Give the preparation type.
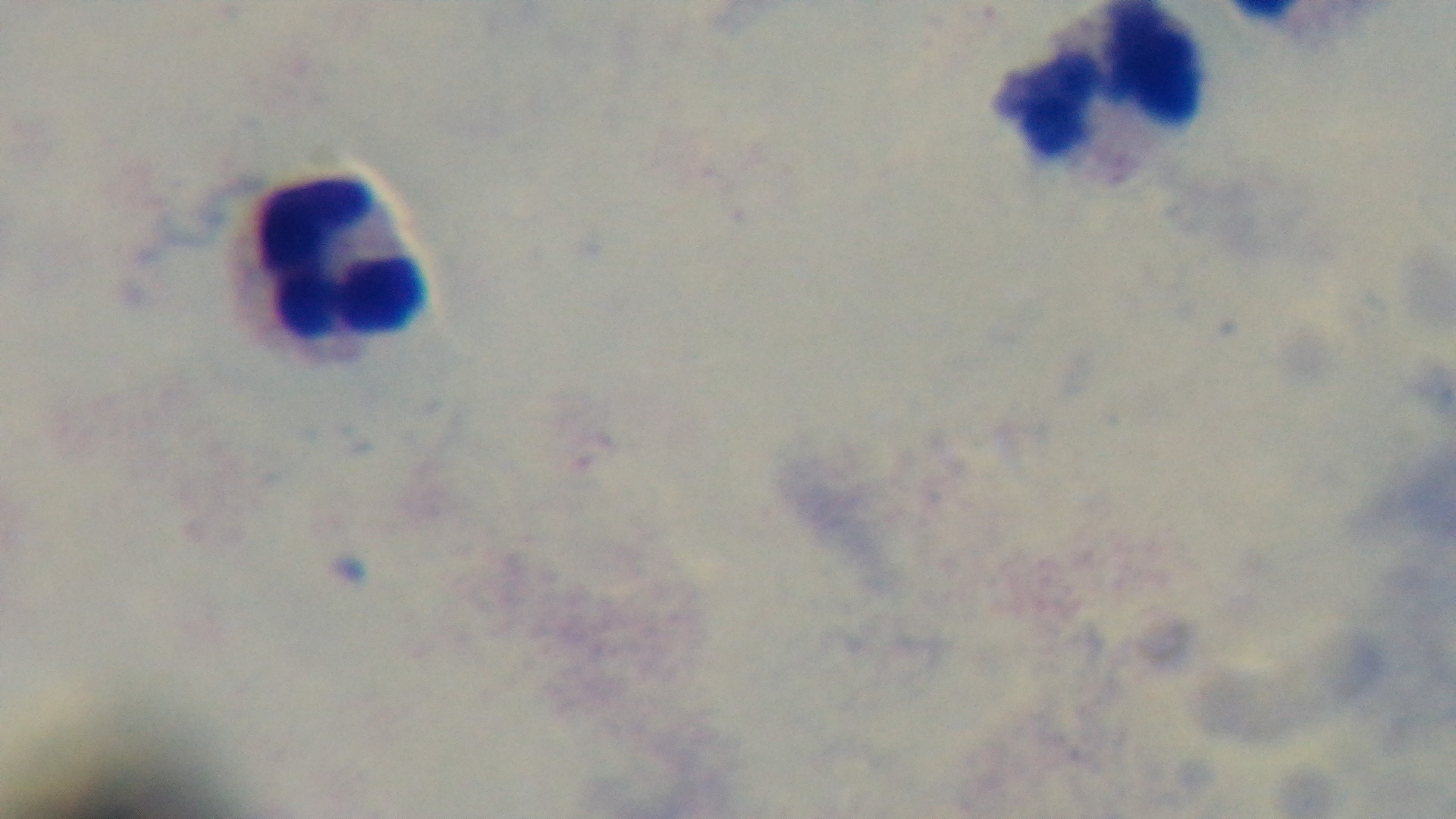
Thick.

{
  "modality": "light microscopy",
  "objective": "100x oil immersion",
  "stain": "Giemsa",
  "field_of_view": "one from the slide",
  "capture": "mounted 4K digital camera",
  "malaria_status": "uninfected"
}